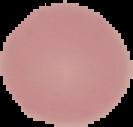
Summary:
  - Image size: 133×127 pixels
  - Image type: segmented cell region on a black background
  - Preparation: thin blood smear
  - Result: no malaria parasites seen